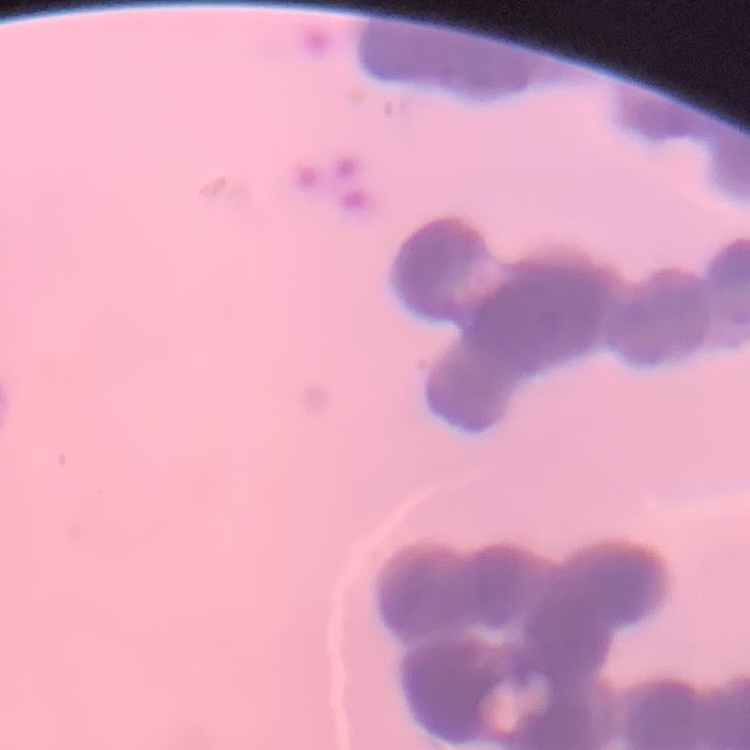
Summary:
  - Red blood cell morphology: rouleaux formation
  - Preparation: thin peripheral smear
  - Stain: Field's or Giemsa
  - Image type: square crop of a larger photomicrograph